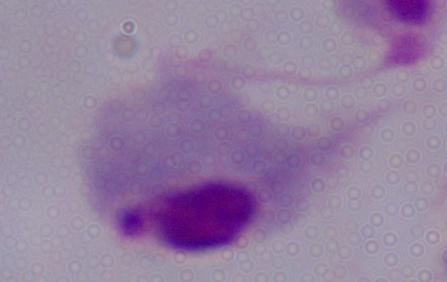 Photomicrograph. A trichomonad is shown. Captured at 1000x magnification.